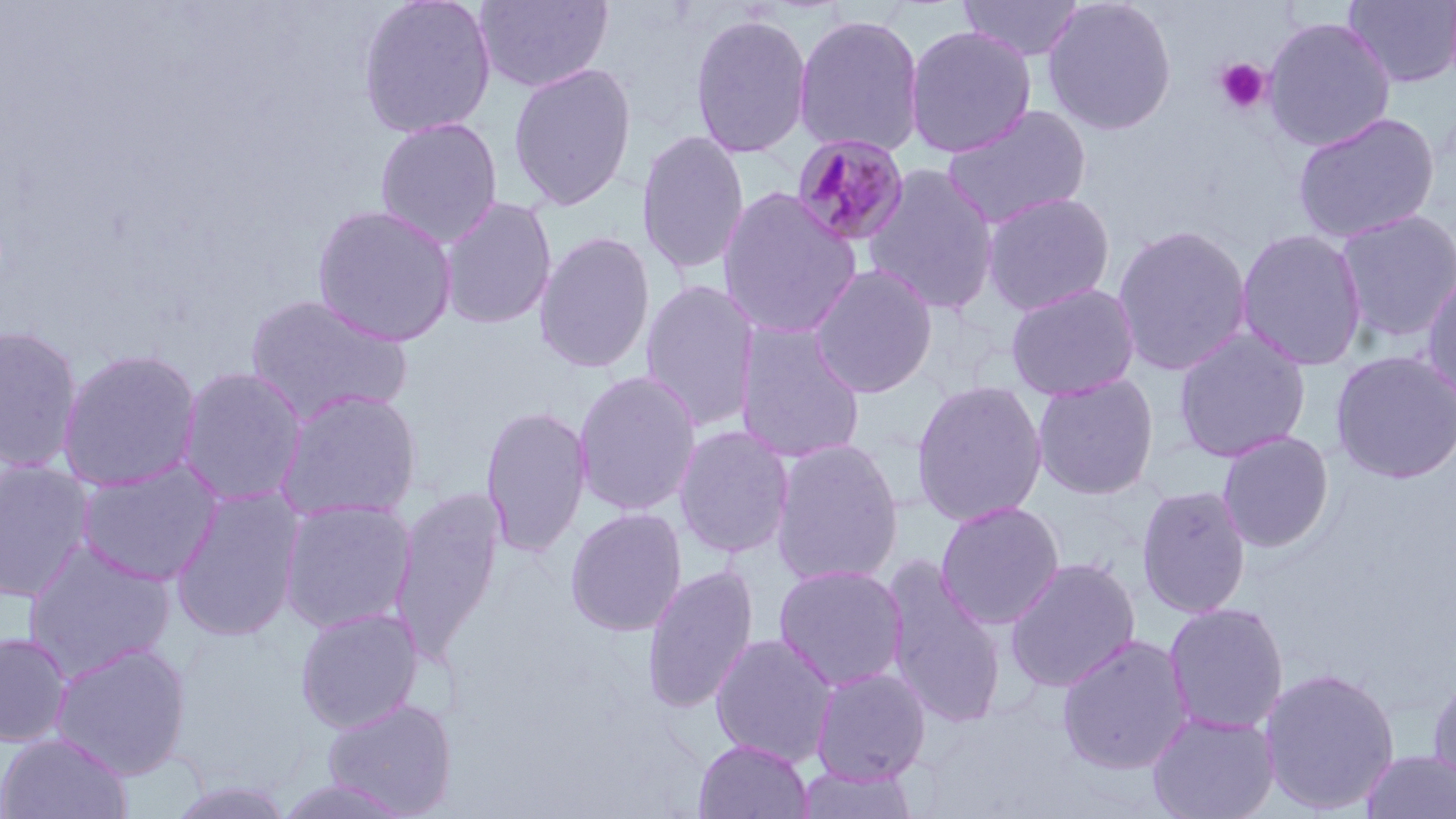
Summary:
  - Coordinate format: approximate bounding boxes as [x1, y1, x2, y2] in pixels
  - Plasmodium malariae-infected red blood cell locations: [791, 132, 911, 247]
  - Platelet locations: [1213, 57, 1270, 115]
  - Uninfected red blood cell locations: [357, 0, 498, 139], [475, 0, 613, 94], [957, 0, 1085, 63], [1041, 0, 1178, 136], [1343, 0, 1456, 89], [689, 12, 813, 159], [792, 13, 926, 158], [1262, 15, 1397, 153], [903, 25, 1038, 159], [507, 62, 637, 211], [940, 103, 1093, 230], [1291, 111, 1441, 245], [374, 117, 503, 248], [635, 129, 751, 277], [861, 163, 1000, 317], [717, 187, 863, 339], [981, 191, 1116, 316], [827, 193, 970, 367], [438, 196, 558, 330], [312, 204, 459, 346], [1334, 209, 1455, 345], [1112, 224, 1253, 376], [1234, 227, 1368, 371], [534, 230, 655, 374], [809, 263, 939, 399], [1420, 264, 1456, 412], [639, 279, 761, 432], [1005, 282, 1141, 400], [244, 293, 413, 426], [734, 321, 868, 464], [0, 324, 84, 473], [1172, 326, 1312, 463], [57, 348, 203, 492], [1330, 349, 1456, 484], [176, 366, 308, 507], [572, 370, 703, 517], [1031, 372, 1160, 500], [910, 379, 1049, 527], [274, 387, 423, 524], [480, 405, 593, 559], [673, 424, 795, 559], [1216, 430, 1335, 553], [769, 438, 905, 587], [74, 458, 225, 587], [0, 459, 96, 603], [1136, 483, 1253, 619], [169, 486, 304, 643], [391, 486, 505, 660], [279, 498, 416, 634], [935, 500, 1066, 630], [565, 507, 687, 636], [22, 540, 177, 680], [1004, 556, 1141, 694], [882, 558, 1008, 730], [773, 563, 909, 691], [642, 564, 759, 713], [1162, 601, 1289, 736], [294, 606, 424, 733], [0, 631, 73, 747], [710, 632, 839, 767], [1056, 633, 1194, 775], [50, 641, 192, 780], [1258, 665, 1401, 815], [809, 666, 932, 785], [1427, 670, 1456, 795], [322, 697, 456, 817], [1146, 710, 1281, 819], [0, 731, 133, 818], [693, 739, 813, 819], [1358, 748, 1456, 819], [792, 763, 923, 819], [273, 776, 417, 819], [165, 780, 297, 818]
  - Slide-level diagnosis: Plasmodium malariae
  - Field of view: single
  - Modality: light microscopy
  - Magnification: 1000x
  - Preparation: thin blood smear
  - Stain: May-Grünwald-Giemsa
  - Image size: 1456×819 pixels